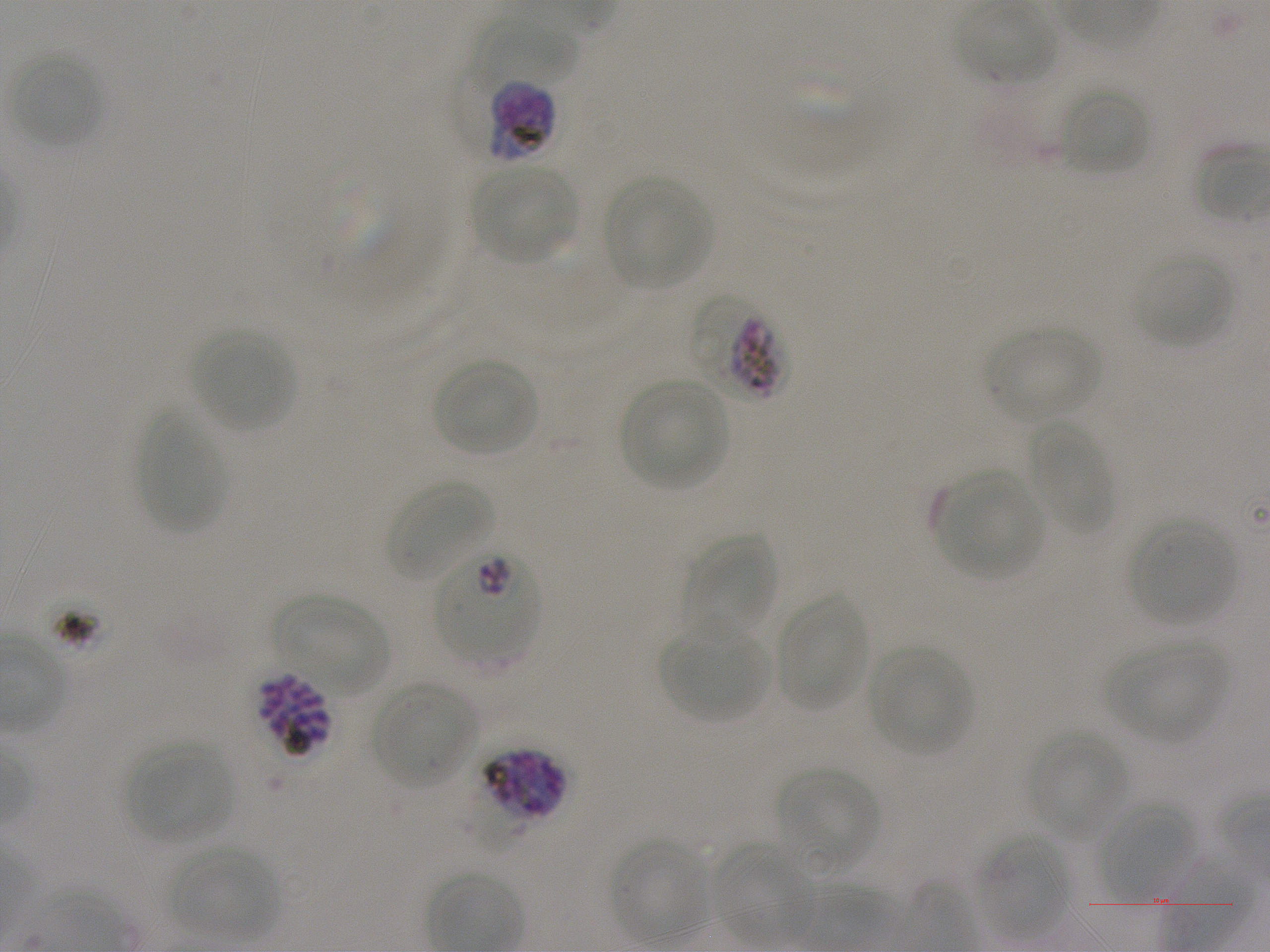

Not every red blood cell is marked. A life-cycle stage — or a range of stages, where the recorded stages span more than one — follows each staged infected red blood cell.
locations of red blood cells of indeterminate infection status = approximate bounding boxes as {x1, y1, x2, y2} in pixels: {777, 59, 883, 161}, {485, 79, 557, 163}, {304, 162, 409, 264}, {689, 294, 785, 402}
culture = in-vitro P. falciparum strain NF54, static
locations of uninfected red blood cells = approximate bounding boxes as {x1, y1, x2, y2} in pixels: {958, 3, 1059, 86}, {470, 16, 581, 93}, {11, 51, 103, 150}, {1059, 86, 1150, 177}, {1194, 144, 1270, 223}, {472, 165, 577, 263}, {602, 176, 713, 289}, {1135, 251, 1234, 349}, {985, 325, 1101, 422}, {190, 329, 296, 431}, {434, 357, 539, 458}, {621, 378, 729, 488}, {137, 410, 227, 534}, {1024, 422, 1112, 534}, {934, 472, 1043, 578}, {388, 478, 493, 580}, {1131, 520, 1237, 626}, {683, 534, 778, 637}, {774, 591, 870, 714}, {275, 592, 389, 695}, {660, 623, 770, 724}, {1108, 640, 1229, 741}, {868, 645, 971, 755}, {371, 683, 476, 787}, {1027, 730, 1127, 836}, {128, 743, 232, 843}, {777, 766, 879, 867}, {1097, 799, 1195, 900}, {979, 834, 1071, 940}, {609, 838, 711, 942}, {711, 843, 814, 945}, {171, 845, 280, 940}
image size = 1270×952 pixels
preparation = thin blood film
donor blood group = A+
stain = Giemsa
field of view = single
locations of infected red blood cells = approximate bounding boxes as {x1, y1, x2, y2} in pixels: {436, 547, 539, 658}; {255, 671, 332, 758} late schizont; {482, 747, 568, 824} schizont
objective = 100x, oil immersion, numerical aperture 1.25